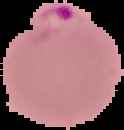

Segmented cell region on a black background. Result: Plasmodium parasites detected. Image is 124×130 pixels. From a thin blood film.